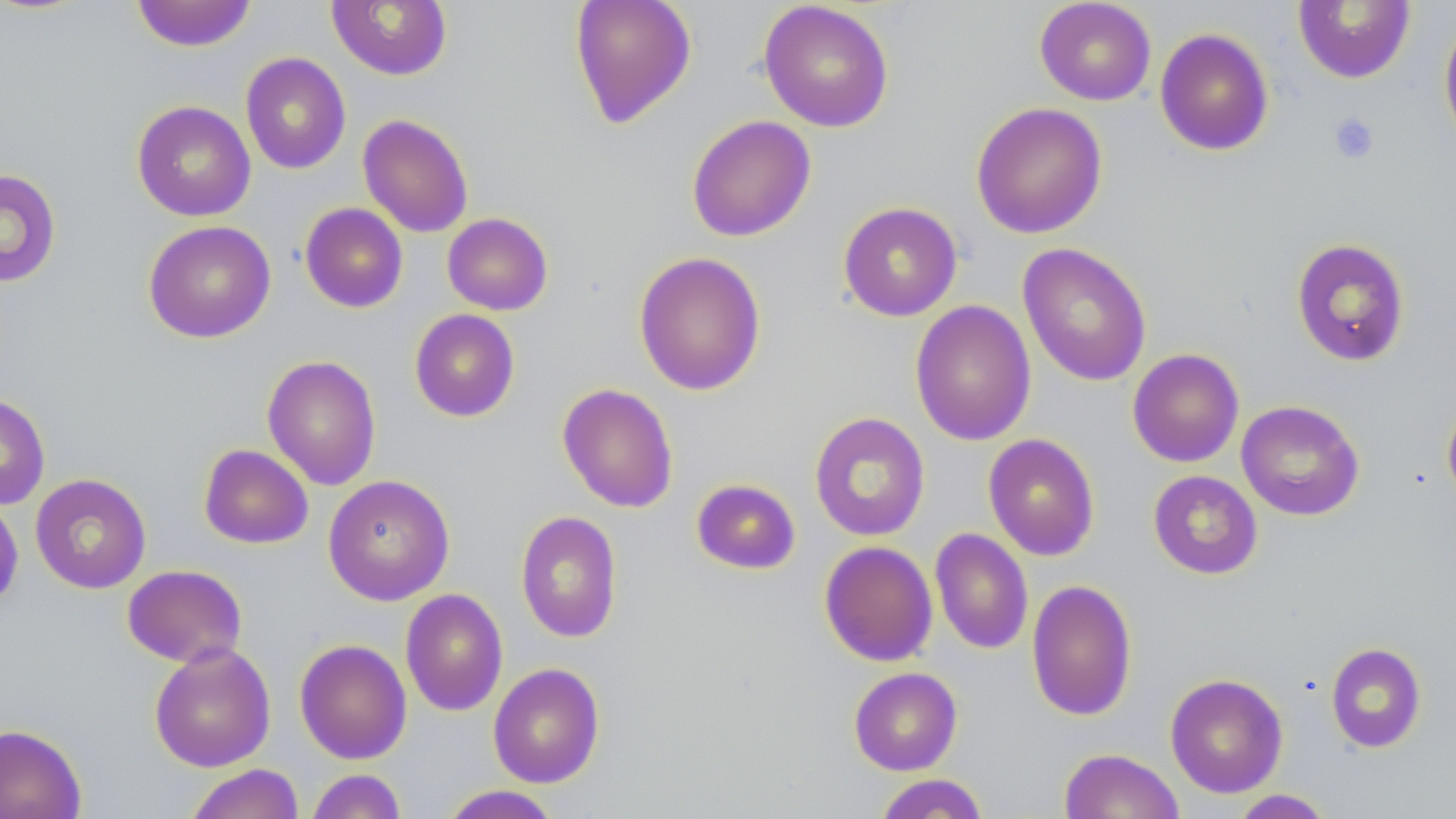

Approximate bounding boxes as (x1, y1, x2, y2) in pixels. Uninfected red blood cell locations: (131, 0, 257, 51), (569, 0, 697, 128), (1035, 0, 1156, 105), (326, 1, 453, 81), (758, 1, 895, 133), (1292, 1, 1416, 84), (1438, 15, 1456, 149), (1154, 27, 1274, 156), (240, 52, 351, 174), (132, 100, 256, 222), (970, 102, 1108, 239), (357, 114, 474, 238), (686, 114, 816, 242), (0, 168, 61, 288), (837, 201, 963, 321), (299, 203, 408, 313), (442, 212, 553, 315), (143, 220, 276, 343), (1291, 237, 1411, 367), (1017, 242, 1152, 387), (633, 251, 766, 396), (910, 300, 1036, 446), (409, 309, 520, 422), (1127, 348, 1244, 467), (262, 355, 382, 491), (557, 383, 679, 513), (0, 393, 50, 510), (1441, 394, 1456, 510), (1236, 400, 1364, 521), (809, 412, 930, 541), (982, 433, 1100, 561), (198, 444, 313, 549), (1148, 470, 1263, 579), (30, 474, 151, 594), (323, 474, 455, 605), (690, 478, 801, 575), (0, 498, 24, 615), (515, 510, 622, 643), (930, 528, 1033, 655), (819, 540, 938, 667), (122, 564, 247, 668), (1026, 578, 1138, 722), (400, 588, 508, 717), (294, 638, 412, 764), (149, 642, 276, 772), (1325, 642, 1427, 753), (488, 662, 605, 788), (848, 667, 963, 775), (1164, 673, 1289, 798), (0, 723, 86, 819), (1058, 747, 1184, 819), (184, 763, 305, 819), (306, 769, 407, 819), (873, 773, 990, 818), (439, 785, 562, 819), (1229, 789, 1336, 819). Platelet locations: (1328, 112, 1380, 164). Slide-level diagnosis: negative for blood parasites. May-Grünwald-Giemsa-stained preparation. Captured at 1000x magnification. Single field of view. Image is 1456×819 pixels. Optical microscopy. Thin blood smear.